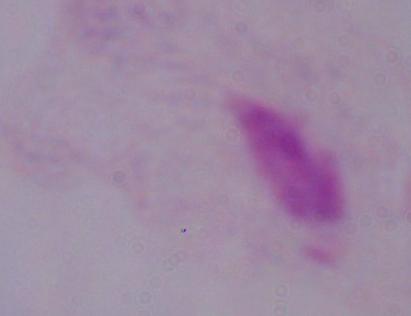

{
  "modality": "micrograph",
  "magnification": "1000x",
  "identification": "trichomonad"
}